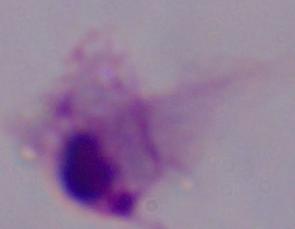

A trichomonad is shown. Captured at 1000x magnification. Micrograph.